Locate every Plasmodium falciparum-infected red blood cell.
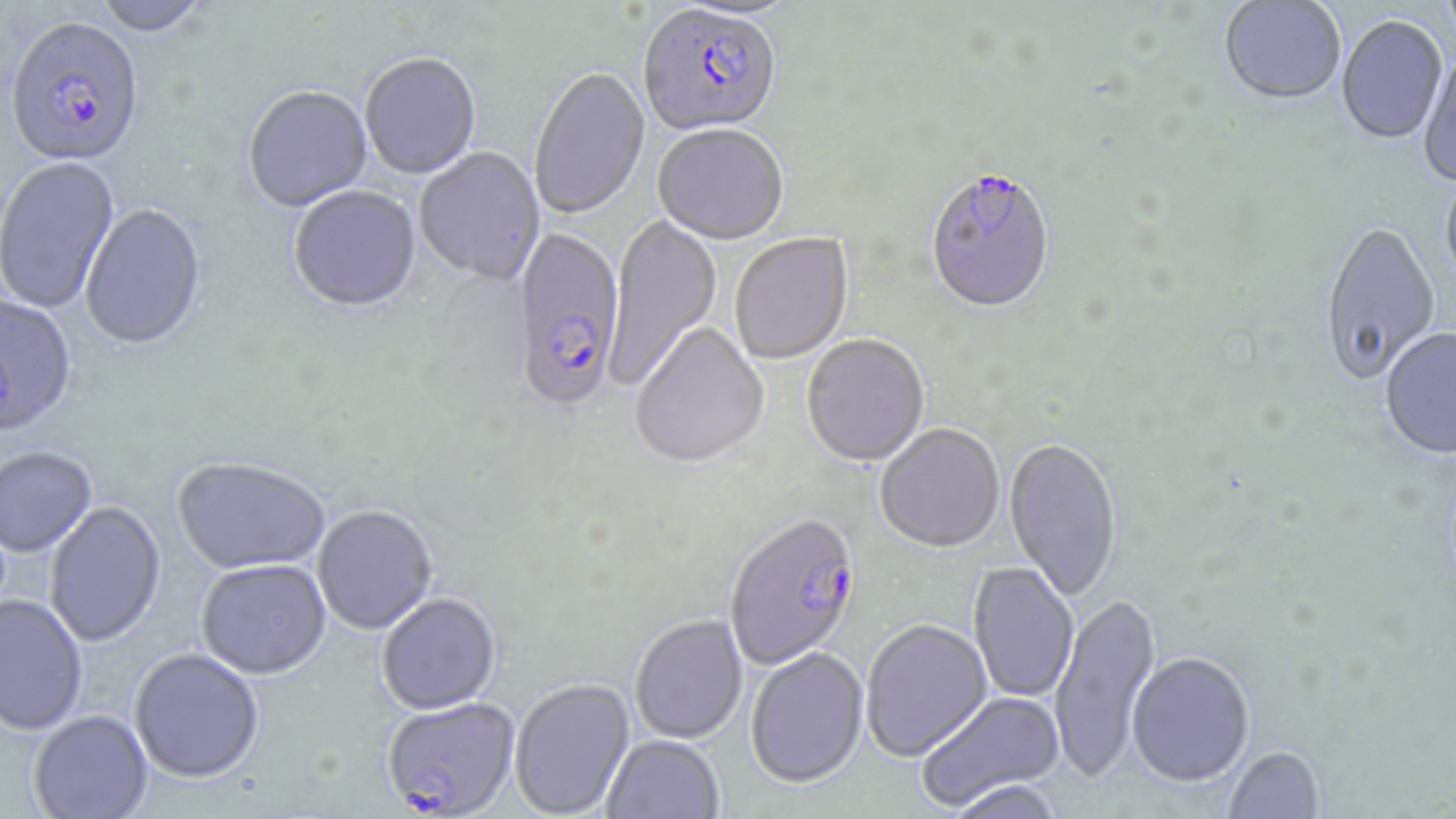

Approximate bounding boxes as [x1, y1, x2, y2] in pixels.
Plasmodium falciparum-infected red blood cells: [638, 7, 783, 140], [5, 20, 145, 171], [924, 172, 1056, 317], [510, 229, 625, 416], [724, 517, 862, 672], [382, 699, 519, 818].

slide-level diagnosis = Plasmodium falciparum
preparation = thin blood film
uninfected red blood cell locations = approximate bounding boxes as [x1, y1, x2, y2] in pixels: [89, 0, 213, 38], [1441, 0, 1456, 45], [1219, 1, 1346, 108], [1337, 17, 1447, 147], [1418, 54, 1456, 188], [360, 55, 481, 181], [528, 69, 650, 221], [243, 88, 373, 214], [653, 127, 789, 248], [414, 148, 545, 288], [0, 157, 120, 314], [1440, 171, 1456, 297], [289, 187, 421, 316], [80, 203, 208, 353], [604, 212, 721, 390], [1318, 223, 1441, 388], [730, 233, 854, 365], [0, 295, 77, 440], [630, 323, 769, 472], [1380, 329, 1456, 461], [802, 336, 929, 469], [875, 426, 1005, 555], [1004, 439, 1122, 606], [0, 449, 96, 558], [172, 459, 330, 577], [45, 501, 166, 649], [312, 507, 438, 637], [196, 562, 331, 681], [968, 562, 1078, 703], [1049, 592, 1161, 785], [0, 595, 88, 736], [377, 595, 501, 716], [629, 615, 748, 744], [860, 619, 992, 763], [745, 647, 869, 789], [129, 650, 264, 784], [1127, 652, 1255, 789], [510, 679, 635, 818], [915, 690, 1064, 812], [28, 711, 153, 819], [602, 735, 724, 819], [1224, 746, 1324, 818], [947, 779, 1064, 819]
modality = light microscopy
stain = May-Grünwald-Giemsa
field of view = single
image size = 1456×819 pixels
magnification = 1000x